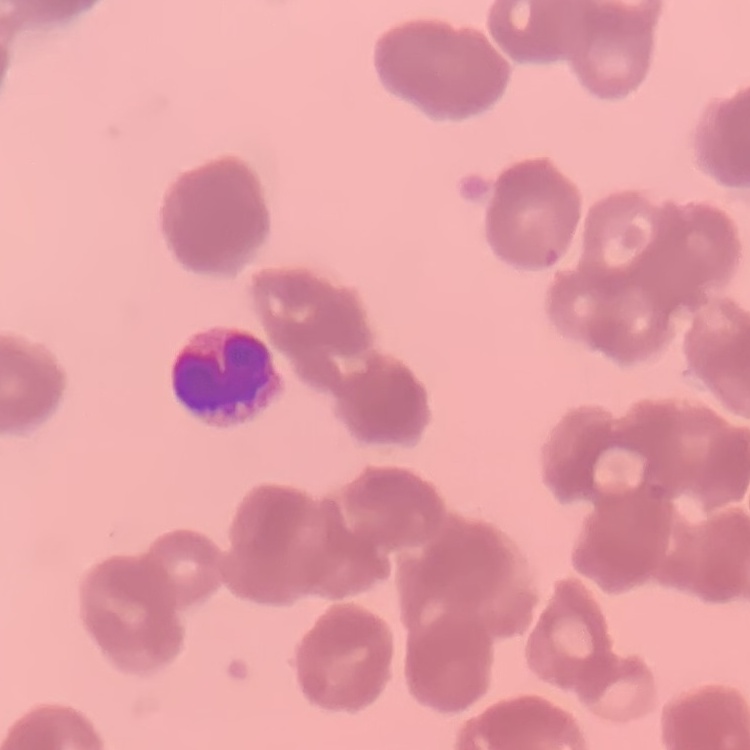
Summary:
  - Erythrocyte morphology: rouleaux formation
  - Image type: one tile cut from a larger photomicrograph
  - Stain: Field's or Giemsa
  - Preparation: thin blood film